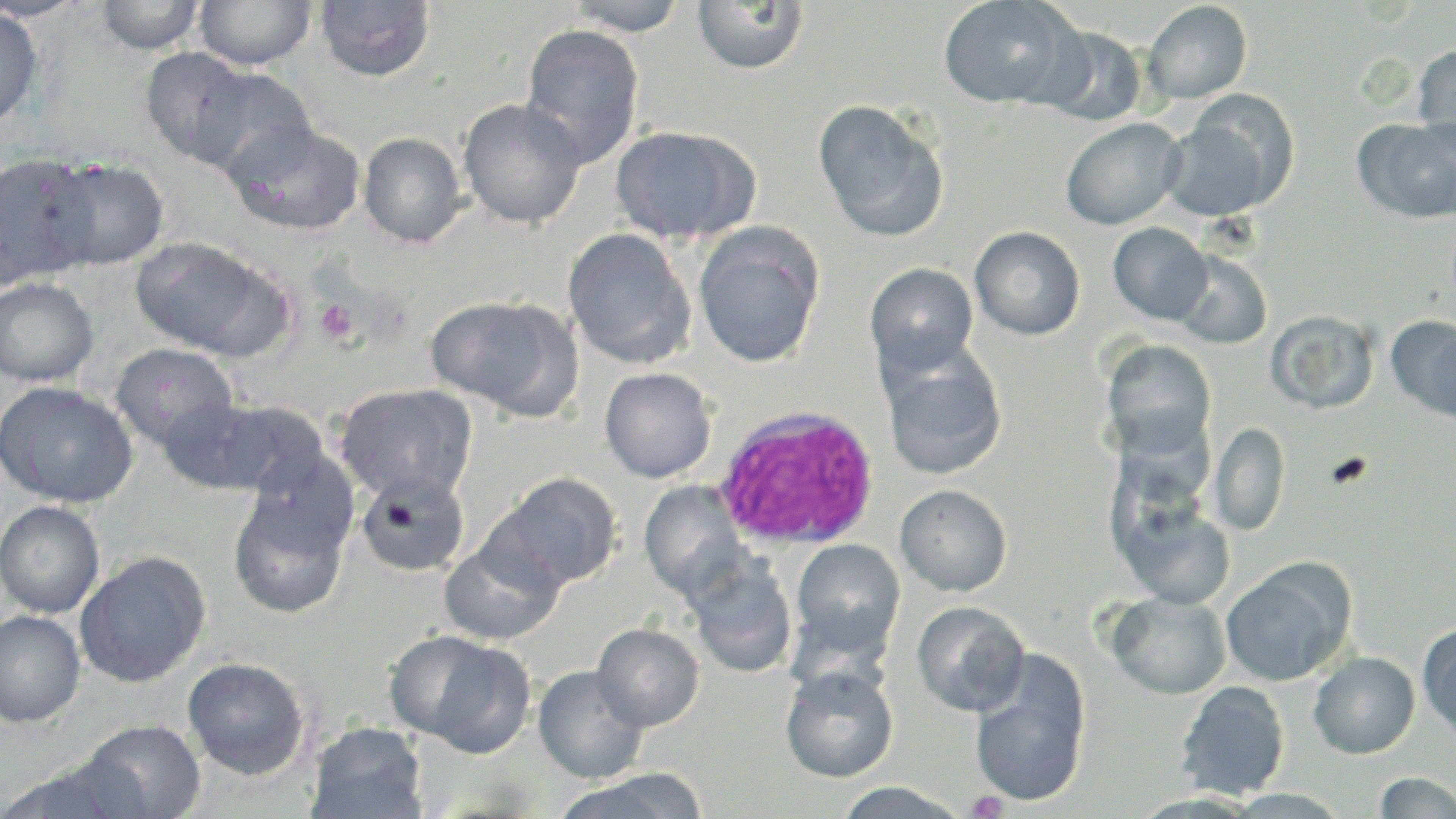

Summary:
  - Coordinate format: approximate bounding boxes as (x1,y1)-(x2,y2) corner pairs in pixels
  - Platelet locations: (314,299)-(359,347), (1323,451)-(1373,491), (966,789)-(1009,818)
  - Uninfected red blood cell locations (subset): (0,0)-(89,22), (96,0)-(205,55), (194,0)-(316,70), (566,0)-(690,37), (937,0)-(1078,109), (315,1)-(436,82), (692,1)-(808,75), (1142,1)-(1252,104), (0,6)-(43,131), (520,23)-(645,168), (1033,24)-(1149,126), (1412,43)-(1456,155), (139,47)-(256,167), (193,67)-(316,180), (458,98)-(586,230), (813,99)-(950,243), (1160,109)-(1285,221), (1061,117)-(1185,230), (1354,117)-(1456,225), (225,122)-(366,236), (609,125)-(758,245), (358,131)-(469,248), (0,152)-(98,287), (46,158)-(170,271), (1108,222)-(1213,325), (692,223)-(826,369), (969,226)-(1085,340), (562,228)-(697,369), (129,236)-(281,358), (1174,250)-(1272,349), (865,262)-(979,379), (0,278)-(99,387), (425,295)-(578,419), (1266,310)-(1379,414), (1388,316)-(1456,424), (1101,340)-(1218,462), (110,342)-(239,451), (880,346)-(1008,481), (599,367)-(717,483), (0,381)-(138,507), (333,383)-(478,504), (155,398)-(269,494), (208,399)-(330,498), (1210,420)-(1289,536), (242,453)-(359,556), (355,471)-(471,579), (499,473)-(623,589), (638,480)-(749,602), (895,483)-(1012,597), (228,492)-(350,618), (1114,498)-(1236,610), (0,500)-(105,618), (439,534)-(566,646), (790,539)-(906,662), (74,551)-(211,687), (1219,558)-(1355,687), (688,559)-(798,679), (1107,591)-(1231,699), (911,600)-(1029,717), (0,610)-(86,728), (592,622)-(705,731), (1417,623)-(1456,742), (418,639)-(535,758), (1308,651)-(1420,758), (969,652)-(1091,808), (182,657)-(311,779), (533,664)-(648,783), (780,664)-(898,783), (1175,680)-(1290,800), (77,719)-(206,819), (307,722)-(429,819), (0,760)-(137,818), (556,770)-(708,819), (1374,772)-(1456,818), (833,782)-(971,817)
  - Slide-level diagnosis: Plasmodium ovale
  - Image size: 1456×819 pixels
  - Magnification: 1000x
  - Preparation: thin blood smear
  - Modality: optical microscopy
  - Field of view: single
  - Stain: May-Grünwald-Giemsa